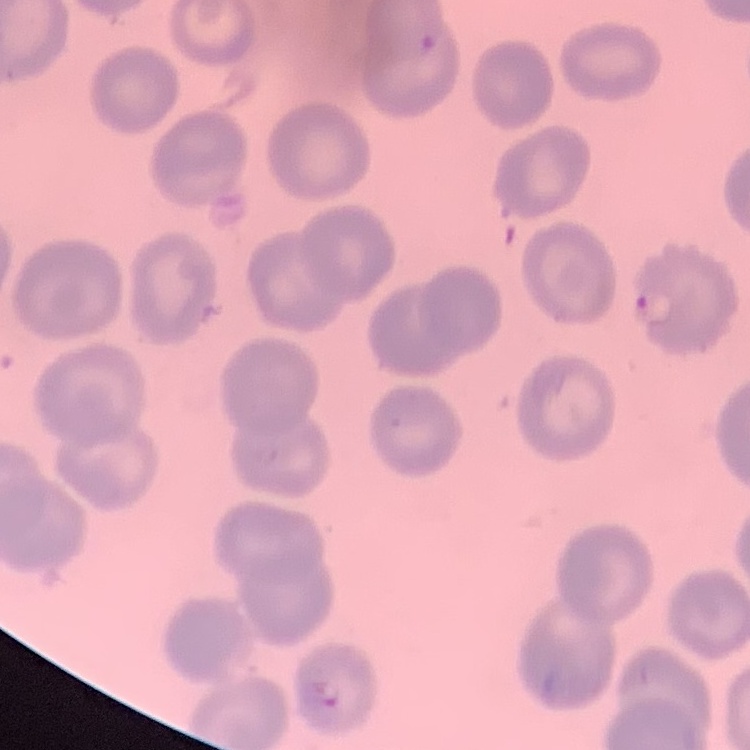
Summary:
  - Erythrocyte morphology: no rouleaux formation
  - Preparation: thin blood film
  - Stain: Field's or Giemsa
  - Image type: one tile cut from a larger photomicrograph